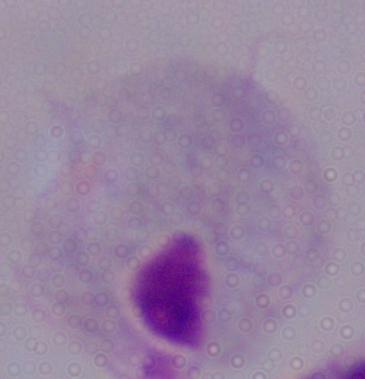

A trichomonad is seen. 1000x magnification. Photomicrograph.